Evaluate for Plasmodium parasites.
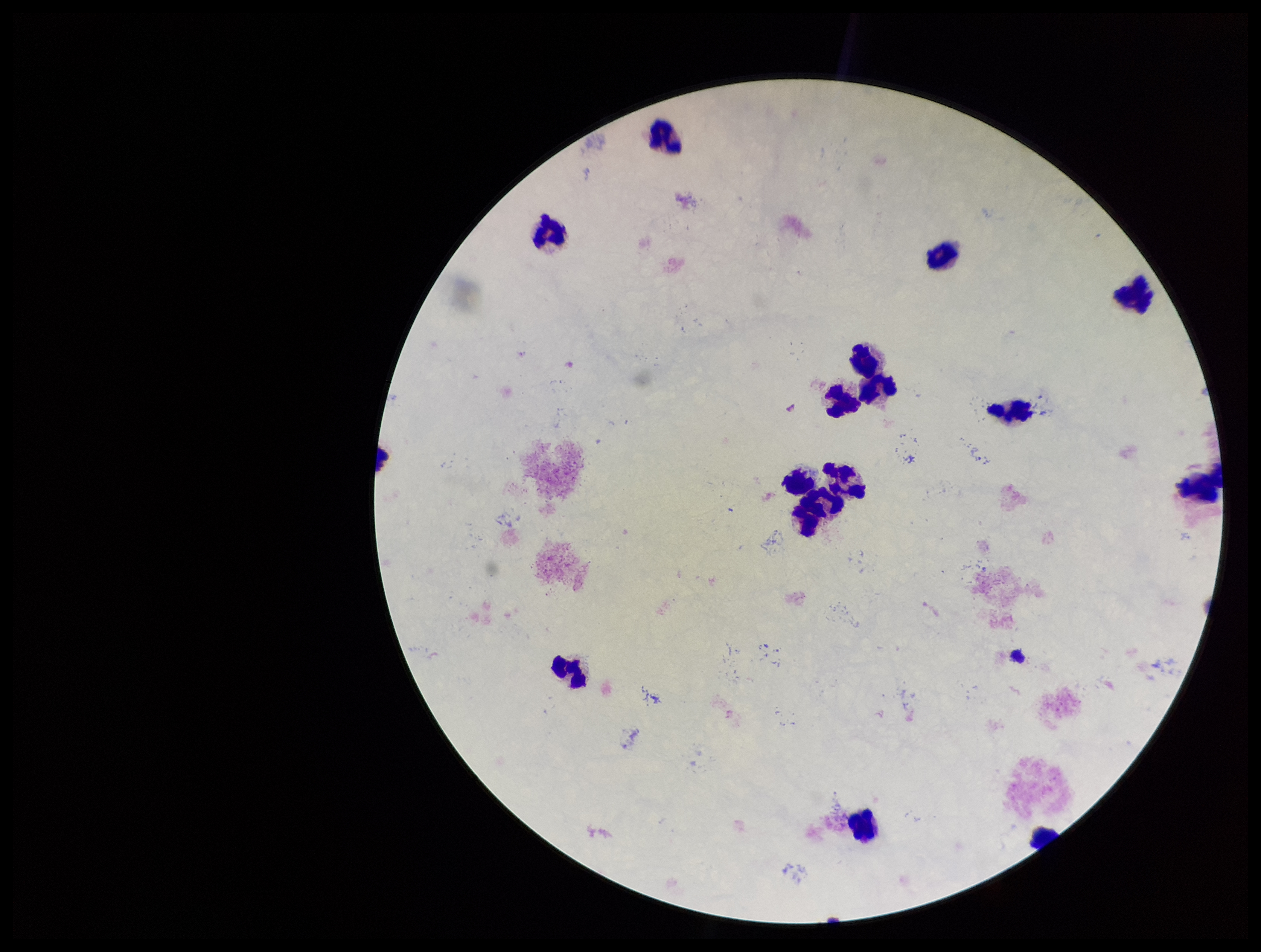
None seen.

Image is 1261×952 pixels. Preparation: thick smear. Parasite count: 0. Patient malaria status: negative. Giemsa stain. Single field of view. Leukocyte count: 14. Smartphone photograph taken through the eyepiece of a microscope.